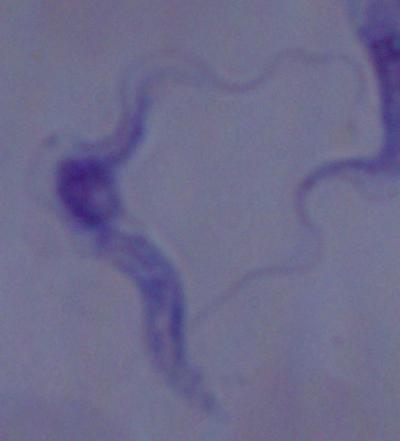 Micrograph. A trypanosome is shown. Captured at 1000x magnification.